Point out each Plasmodium parasite.
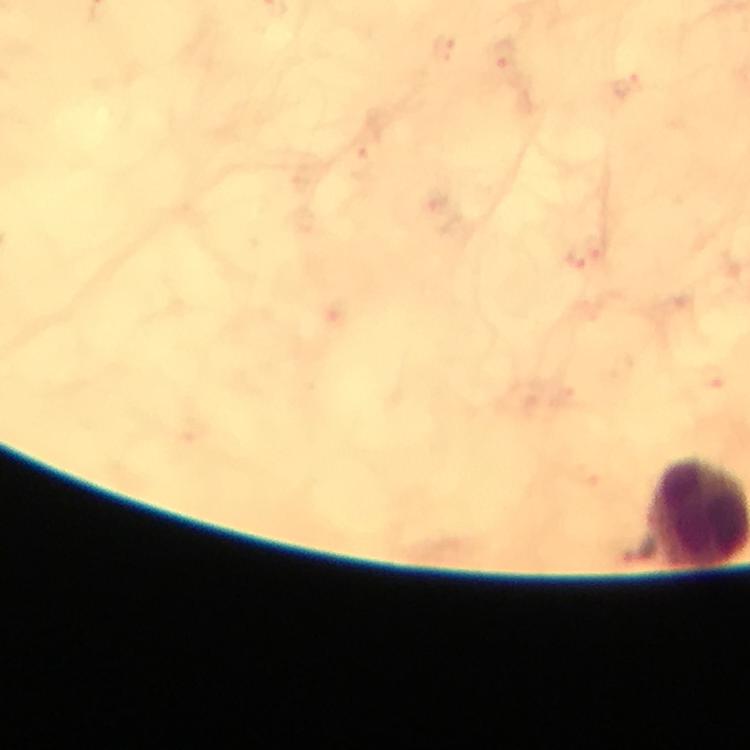

Approximate centers as {x, y} in pixels.
Plasmodium parasites: {505, 54}.

Summary:
  - Magnification: 100x
  - Context: from a diagnostic examination for malaria
  - Cropped from: a single field of view
  - Preparation: thick blood film
  - Image size: 750×750 pixels
  - Stain: Giemsa
  - Capture: smartphone mounted on the microscope
  - Immersion oil: applied